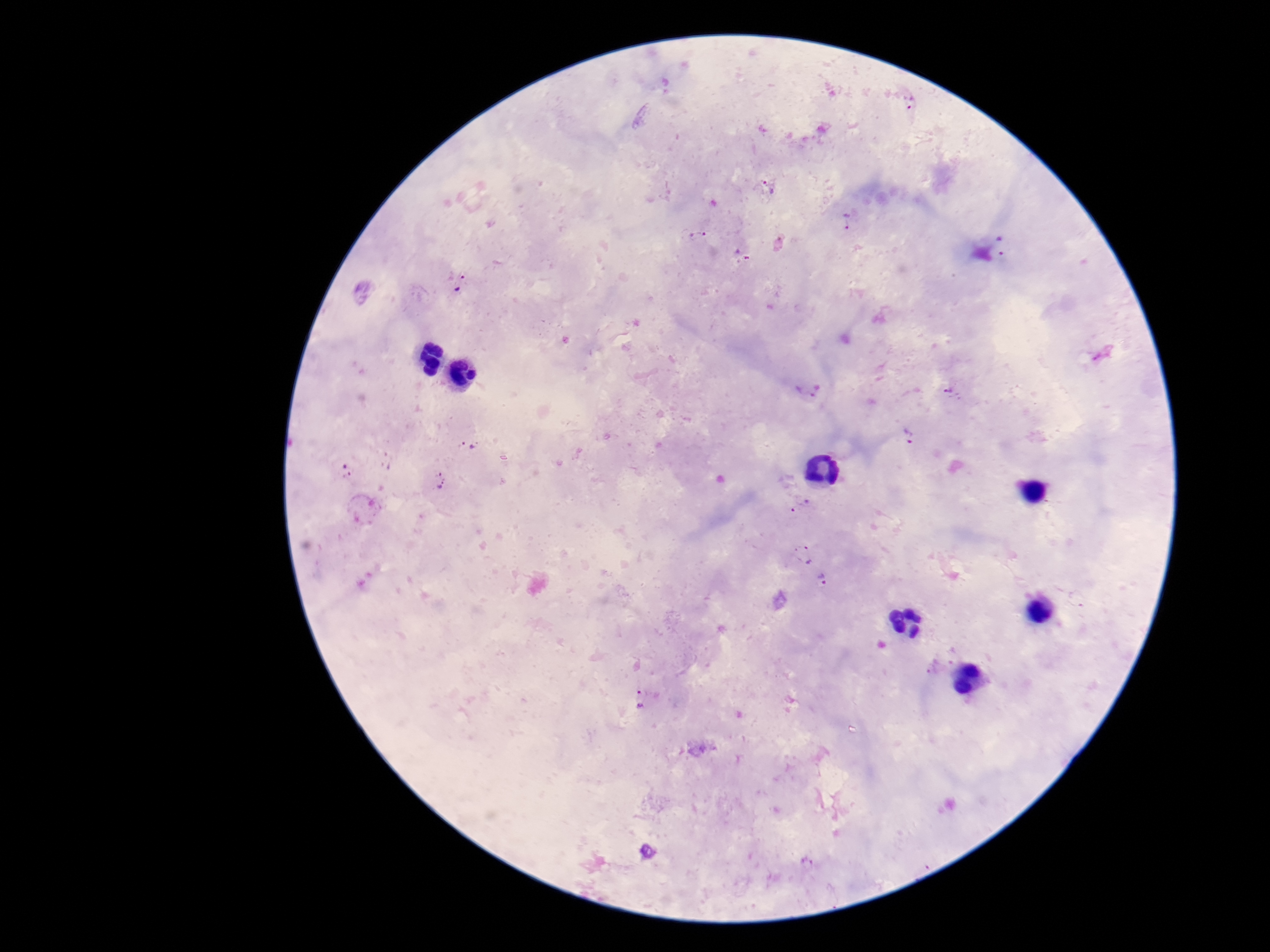 Approximate centers as {x, y} in pixels. Plasmodium parasite locations: {912, 102}, {768, 187}, {846, 221}, {697, 234}, {1001, 246}, {460, 282}, {808, 391}, {950, 392}, {909, 437}, {467, 446}, {346, 471}, {440, 481}, {800, 507}, {802, 555}, {823, 581}, {641, 700}, {647, 852}. Smartphone photograph taken through the microscope eyepiece. Giemsa stain. Patient malaria status: infected. 100x magnification. Thick blood smear. Image is 1270×952 pixels. Single field of view.